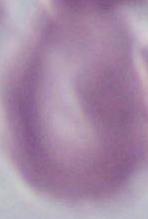

1000x magnification. An erythrocyte is seen. Photomicrograph.